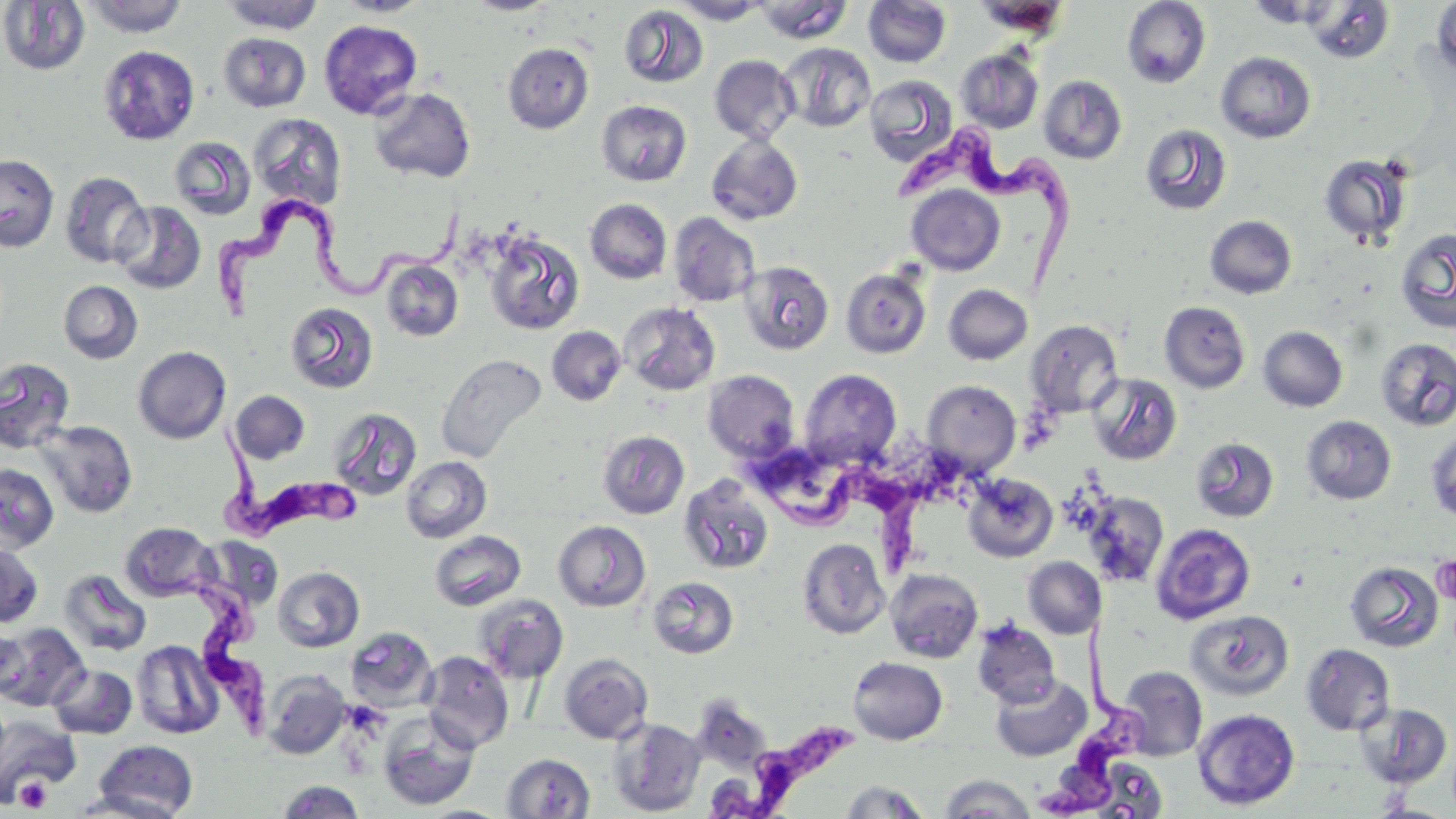
Summary:
  - Coordinate format: approximate bounding boxes as (x1,y1)-(x2,y2) corner pairs in pixels
  - Platelet locations: (1431,554)-(1456,604), (14,775)-(53,812)
  - Uninfected red blood cell locations: (82,0)-(188,37), (220,0)-(326,34), (335,0)-(432,17), (465,0)-(557,15), (972,0)-(1070,38), (1432,0)-(1456,81), (0,1)-(90,76), (671,1)-(770,25), (753,1)-(852,43), (863,1)-(951,68), (1122,1)-(1211,89), (1302,2)-(1396,64), (618,5)-(709,88), (318,19)-(423,120), (218,32)-(311,112), (503,43)-(594,134), (778,43)-(876,133), (97,45)-(200,146), (955,48)-(1044,134), (1215,51)-(1316,144), (709,55)-(799,144), (865,75)-(959,168), (1038,75)-(1127,164), (368,87)-(476,184), (596,100)-(692,186), (248,113)-(347,210), (1140,124)-(1232,216), (706,134)-(803,225), (169,136)-(257,221), (1318,153)-(1415,247), (0,154)-(60,253), (60,171)-(152,269), (906,184)-(1005,276), (585,198)-(672,285), (112,201)-(206,295), (668,212)-(760,307), (1205,215)-(1297,299), (1395,228)-(1456,334), (482,230)-(586,336), (380,258)-(464,342), (738,260)-(835,356), (841,267)-(931,359), (58,280)-(143,364), (943,284)-(1033,365), (619,301)-(721,396), (1159,301)-(1251,394), (285,302)-(379,395), (1025,319)-(1124,418), (547,326)-(626,406), (1258,326)-(1348,412), (1375,337)-(1456,432), (132,346)-(231,444), (436,353)-(547,464), (0,357)-(76,454), (798,369)-(902,469), (703,370)-(800,463), (1087,372)-(1183,465), (921,380)-(1021,477), (230,390)-(310,464), (327,407)-(423,502), (1302,415)-(1396,505), (35,420)-(138,518), (1426,427)-(1456,525), (598,430)-(689,519), (1191,436)-(1280,522), (401,456)-(492,543), (0,464)-(59,553), (963,474)-(1058,563), (678,475)-(774,575), (1082,492)-(1169,587), (553,520)-(651,612), (120,522)-(218,602), (1151,523)-(1256,624), (428,530)-(527,611), (198,536)-(284,611), (797,538)-(890,639), (0,543)-(43,627), (1023,556)-(1104,639), (1345,561)-(1444,652), (273,566)-(365,652), (59,568)-(152,657), (885,568)-(983,662), (648,576)-(739,659), (472,593)-(569,683), (1186,610)-(1294,701), (972,620)-(1060,708), (0,623)-(90,712), (345,626)-(438,712), (0,627)-(27,697), (131,639)-(224,739), (1301,642)-(1396,736), (420,651)-(514,752), (559,653)-(653,743), (848,656)-(948,745), (47,663)-(138,739), (1117,665)-(1207,761), (260,669)-(351,759), (990,674)-(1092,762), (1357,702)-(1453,789), (1192,708)-(1300,810), (377,711)-(479,811), (1,714)-(78,804), (608,717)-(706,816), (91,740)-(200,818), (502,753)-(595,818), (1088,757)-(1169,818), (939,774)-(1037,818), (278,780)-(364,817), (838,780)-(932,818), (70,789)-(189,819)
  - Trypanosoma brucei locations: (898,118)-(1078,298), (206,188)-(469,321), (217,418)-(363,548), (743,451)-(925,573), (130,570)-(284,746), (1035,625)-(1148,819), (711,733)-(847,817)
  - Slide-level diagnosis: Trypanosoma brucei
  - Stain: May-Grünwald-Giemsa
  - Field of view: one of a larger specimen
  - Modality: optical microscopy
  - Preparation: thin blood smear
  - Image size: 1456×819 pixels
  - Magnification: 1000x